State which parasite is depicted.
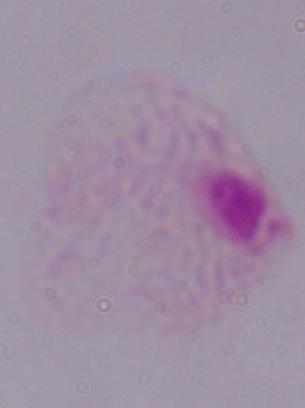

A trichomonad.

Captured at 1000x magnification. Photomicrograph.